Name the parasite shown.
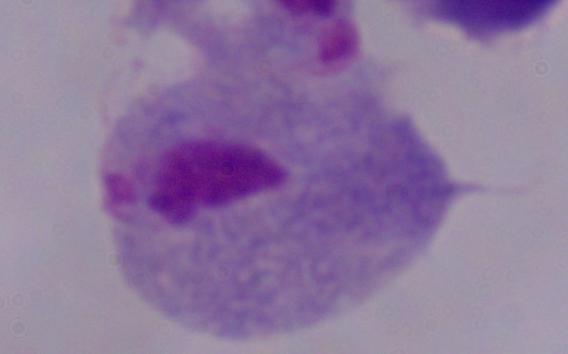

This is a trichomonad.

Summary:
  - Magnification: 1000x
  - Modality: micrograph